Outline each Plasmodium ovale-infected red blood cell.
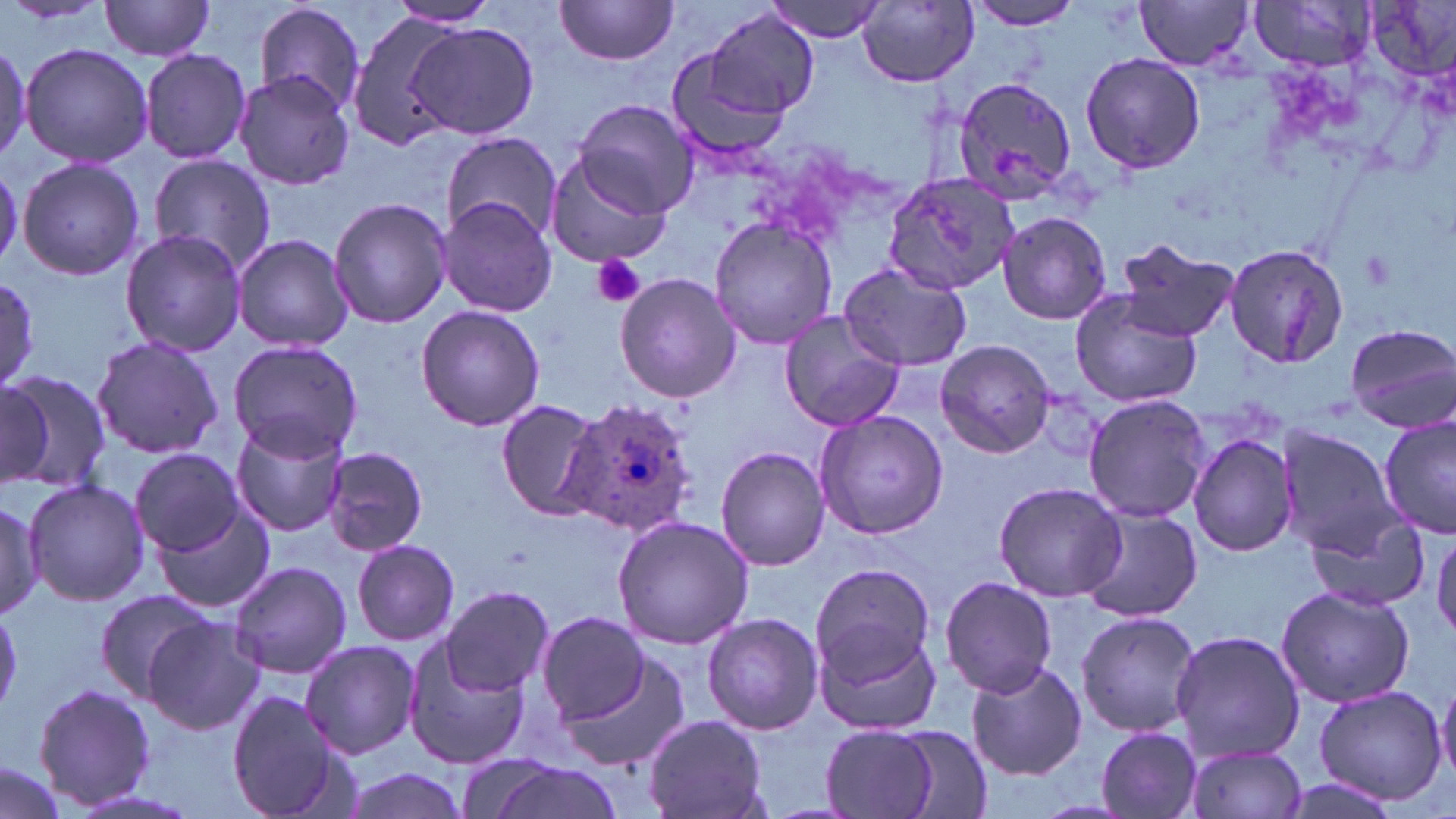

Approximate bounding boxes as [x1, y1, x2, y2] in pixels.
Plasmodium ovale-infected red blood cells: [567, 400, 699, 540].

slide-level diagnosis = Plasmodium ovale
field of view = one of a larger specimen
uninfected red blood cell locations = approximate bounding boxes as [x1, y1, x2, y2] in pixels: [98, 0, 219, 60], [761, 0, 886, 42], [971, 0, 1084, 32], [1134, 0, 1256, 69], [1249, 0, 1378, 70], [553, 1, 681, 65], [855, 1, 979, 88], [251, 3, 366, 114], [385, 3, 503, 29], [348, 10, 464, 150], [707, 10, 820, 118], [408, 22, 540, 140], [21, 43, 153, 170], [140, 48, 252, 165], [663, 48, 791, 162], [1080, 51, 1207, 174], [233, 70, 356, 192], [951, 74, 1080, 203], [574, 100, 698, 217], [443, 133, 561, 244], [543, 147, 676, 271], [146, 153, 276, 278], [16, 157, 147, 281], [884, 171, 1021, 294], [328, 196, 450, 329], [438, 197, 558, 317], [997, 212, 1111, 325], [708, 217, 839, 350], [119, 228, 246, 357], [233, 232, 353, 351], [1110, 238, 1238, 344], [1221, 241, 1353, 368], [837, 259, 974, 373], [0, 273, 40, 388], [615, 273, 740, 402], [1069, 289, 1207, 408], [415, 305, 546, 431], [777, 311, 905, 432], [1346, 323, 1456, 431], [90, 335, 224, 461], [228, 340, 364, 460], [934, 340, 1056, 457], [0, 369, 112, 491], [0, 380, 53, 488], [1083, 393, 1211, 523], [496, 399, 607, 521], [814, 407, 953, 540], [1379, 410, 1455, 538], [229, 419, 350, 537], [1275, 425, 1400, 555], [1187, 430, 1300, 556], [323, 446, 430, 557], [131, 447, 244, 556], [717, 447, 830, 571], [23, 478, 151, 609], [994, 482, 1127, 602], [0, 497, 43, 622], [155, 507, 276, 614], [1079, 508, 1204, 623], [1302, 511, 1429, 613], [611, 515, 756, 650], [1431, 530, 1456, 640], [351, 540, 461, 647], [227, 559, 353, 680], [811, 562, 935, 679], [939, 576, 1059, 698], [1275, 584, 1415, 709], [97, 587, 217, 704], [443, 587, 555, 697], [0, 600, 22, 714], [1074, 609, 1202, 738], [700, 612, 825, 735], [537, 613, 650, 724], [143, 614, 265, 736], [815, 619, 944, 735], [1170, 630, 1306, 762], [404, 637, 529, 772], [299, 639, 419, 757], [559, 656, 692, 769], [965, 661, 1087, 781], [1436, 676, 1456, 783], [38, 681, 155, 807], [1313, 685, 1448, 807], [227, 690, 348, 818], [643, 713, 771, 819], [818, 725, 947, 819], [1095, 727, 1203, 818], [881, 728, 995, 818], [1183, 742, 1308, 819], [457, 753, 567, 819], [0, 759, 68, 819], [484, 763, 627, 819], [342, 768, 471, 819]
magnification = 1000x
image size = 1456×819 pixels
platelet locations = approximate bounding boxes as [x1, y1, x2, y2] in pixels: [1358, 247, 1398, 290], [590, 253, 647, 309]
modality = optical microscopy
stain = May-Grünwald-Giemsa
preparation = thin blood smear